Identify the parasite.
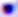
Toxoplasma gondii.

400x magnification. Photomicrograph.